Locate and identify every blood parasite.
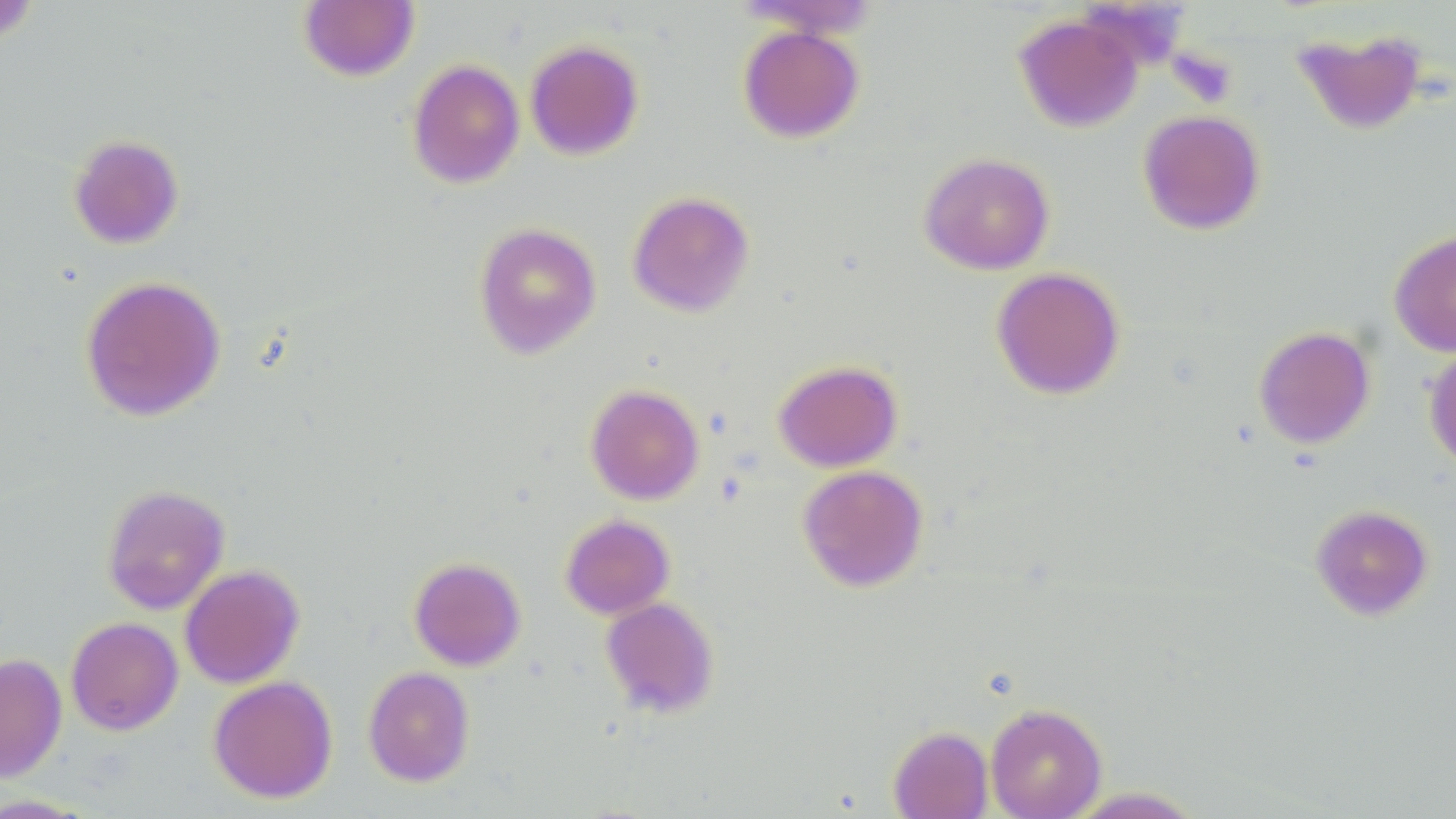

No blood parasites observed.

slide-level diagnosis = no evidence of blood parasites
field of view = one of a larger specimen
uninfected red blood cell locations = approximate bounding boxes as (x1,y1)-(x2,y2) corner pairs in pixels: (0,1)-(42,46), (297,1)-(420,82), (1014,14)-(1143,133), (737,24)-(865,143), (1290,27)-(1429,136), (524,39)-(645,161), (406,58)-(525,189), (1137,109)-(1266,235), (67,133)-(184,249), (918,151)-(1055,275), (627,190)-(755,317), (473,222)-(602,359), (1389,229)-(1456,357), (991,266)-(1126,400), (80,274)-(226,422), (1253,326)-(1376,449), (1423,341)-(1456,474), (773,359)-(903,472), (585,383)-(705,505), (797,464)-(929,593), (101,484)-(230,615), (1309,504)-(1435,622), (560,513)-(675,620), (408,556)-(526,671), (179,564)-(305,689), (600,597)-(720,718), (65,616)-(183,735), (0,653)-(67,782), (363,666)-(475,787), (207,675)-(338,803), (985,702)-(1107,819), (887,725)-(994,819), (1060,786)-(1208,818)
modality = optical microscopy
platelet locations = approximate bounding boxes as (x1,y1)-(x2,y2) corner pairs in pixels: (1,3)-(40,44), (1169,48)-(1238,107)
magnification = 1000x
stain = May-Grünwald-Giemsa
preparation = thin blood smear
image size = 1456×819 pixels